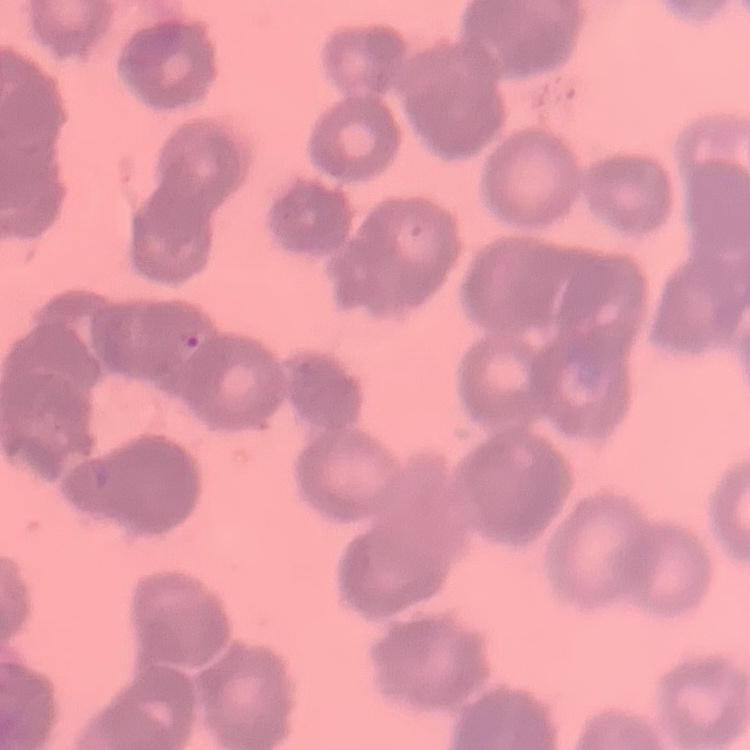

erythrocyte morphology = rouleaux formation
image type = square crop of a larger photomicrograph
preparation = thin blood smear
stain = Field's or Giemsa